Report the malaria status of this cell.
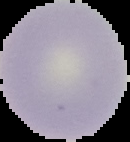

It is uninfected.

Summary:
  - Image size: 130×142 pixels
  - Preparation: thin blood film
  - Image type: segmented cell region with the area outside set to black